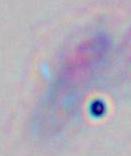

Toxoplasma gondii is seen. Captured at 1000x magnification. Micrograph.